Classify the preparation.
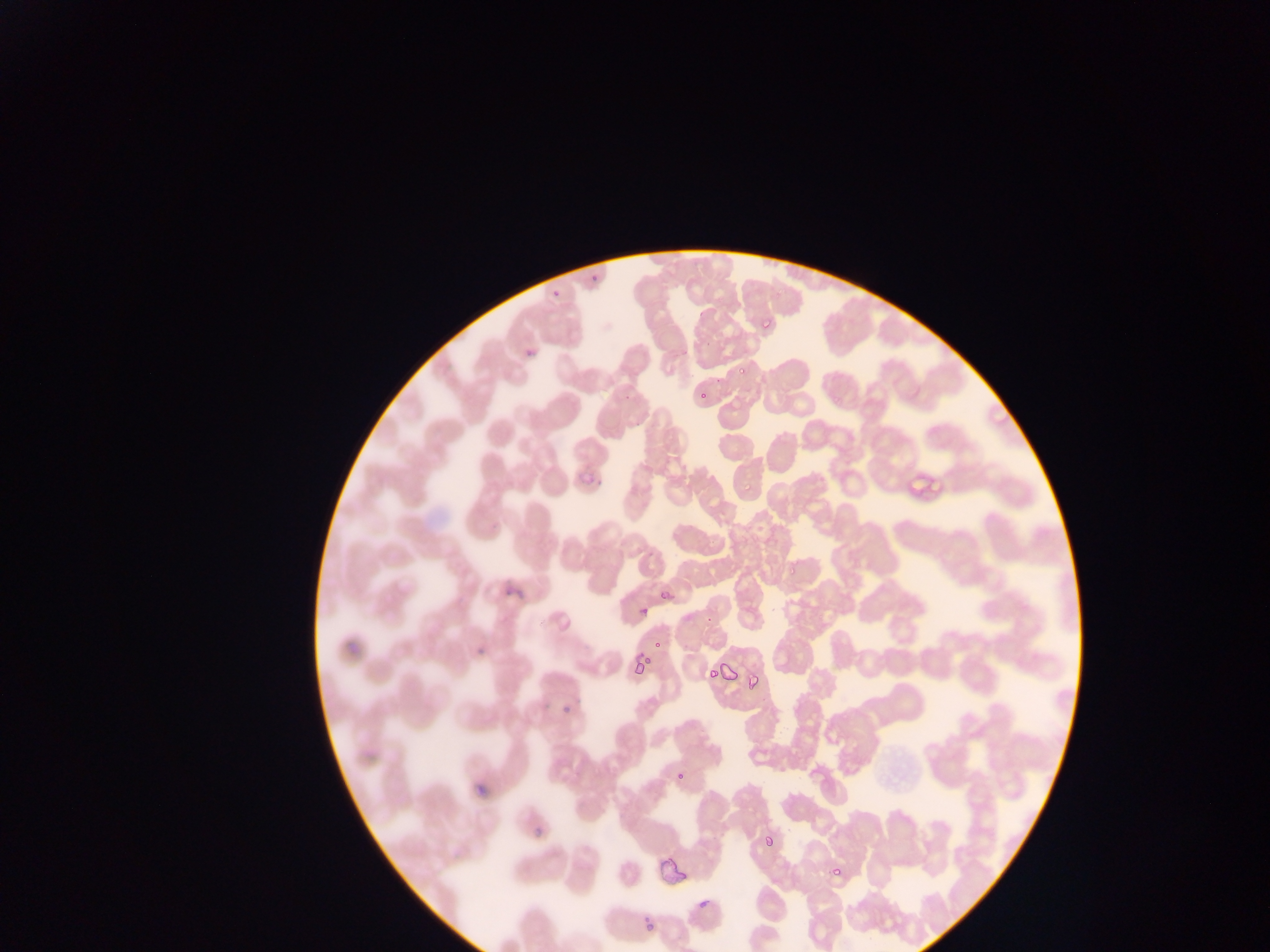
Thin blood smear.

Approximate bounding boxes as [left, top, right, bottom] in pixels. Malaria parasite locations: [590, 269, 609, 282], [546, 285, 557, 298], [751, 322, 769, 333], [521, 339, 545, 356], [735, 363, 748, 376], [695, 384, 720, 404], [915, 469, 958, 504], [580, 472, 604, 492], [731, 476, 748, 500], [784, 564, 802, 577], [503, 568, 527, 598], [661, 586, 674, 604], [635, 604, 654, 624], [347, 631, 368, 655], [472, 632, 486, 655], [649, 639, 669, 651], [632, 652, 661, 679], [720, 660, 739, 691], [707, 667, 718, 680], [740, 675, 758, 690], [560, 709, 573, 719], [354, 740, 389, 762], [475, 770, 500, 808], [675, 772, 696, 785], [529, 805, 557, 844], [762, 825, 779, 847], [646, 848, 704, 893], [829, 863, 844, 879], [697, 897, 712, 910], [636, 911, 669, 944]. One field of view. Photographed through a microscope with a mobile-phone camera. Collected in Ghana. Image is 1270×952 pixels.